Outline each blood parasite and name the species.
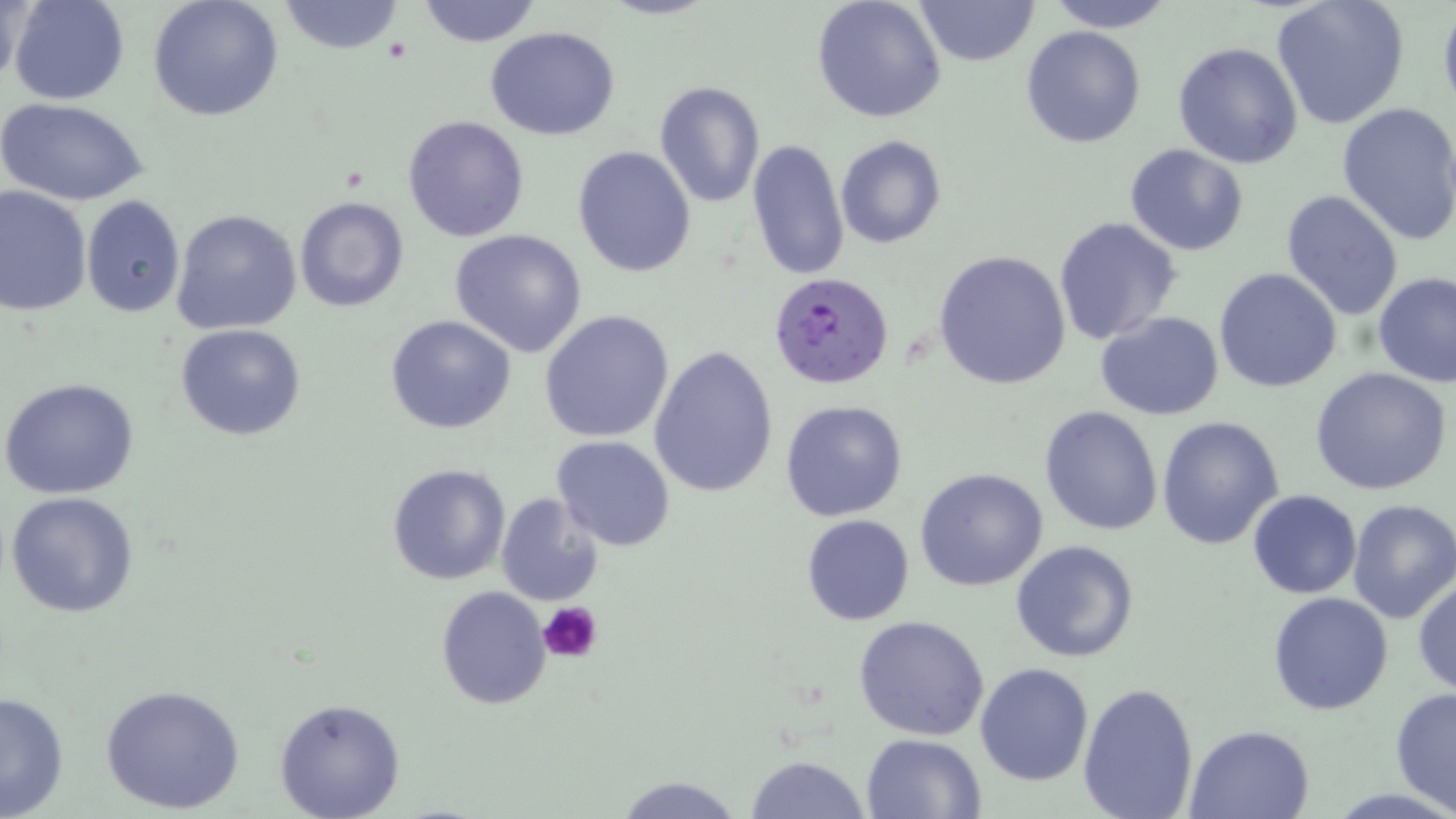
Approximate bounding boxes as (x1, y1, x2, y2) in pixels.
Plasmodium falciparum-infected red blood cells: (770, 272, 893, 390).
No Plasmodium ovale, Plasmodium malariae, Plasmodium vivax, Babesia divergens, or Trypanosoma brucei observed.

Uninfected red blood cell locations: (2, 0, 31, 85), (8, 0, 129, 106), (148, 0, 284, 122), (276, 0, 408, 54), (415, 0, 542, 48), (812, 0, 948, 123), (913, 0, 1040, 67), (1045, 0, 1177, 32), (1270, 0, 1410, 130), (1437, 2, 1456, 123), (484, 26, 623, 141), (1021, 26, 1147, 149), (1173, 41, 1303, 169), (653, 80, 765, 209), (1, 96, 150, 207), (1337, 101, 1456, 244), (402, 116, 530, 241), (834, 134, 946, 247), (745, 138, 850, 282), (1125, 144, 1250, 255), (572, 145, 697, 278), (0, 185, 93, 317), (1279, 189, 1403, 323), (294, 195, 410, 313), (81, 196, 185, 317), (171, 207, 302, 336), (1053, 217, 1182, 345), (449, 228, 588, 357), (933, 249, 1072, 390), (1214, 267, 1343, 393), (1373, 271, 1455, 387), (540, 310, 674, 444), (1095, 311, 1223, 421), (385, 315, 517, 435), (176, 324, 308, 441), (649, 343, 779, 498), (1310, 366, 1454, 497), (1, 379, 141, 500), (780, 399, 908, 521), (1039, 405, 1164, 536), (1156, 415, 1284, 550), (551, 436, 675, 552), (386, 463, 511, 586), (915, 468, 1049, 592), (5, 490, 140, 618), (1247, 490, 1361, 599), (495, 492, 607, 608), (1346, 498, 1456, 625), (801, 514, 915, 625), (1011, 539, 1141, 663), (1413, 577, 1456, 697), (434, 586, 552, 708), (1267, 591, 1394, 716), (853, 614, 990, 740), (974, 663, 1093, 786), (1077, 680, 1200, 818), (99, 683, 246, 815), (1390, 686, 1456, 817), (0, 689, 70, 819), (274, 697, 405, 819), (1184, 723, 1316, 817), (862, 733, 986, 819), (744, 754, 873, 818), (613, 775, 744, 818). Platelet locations: (538, 602, 603, 664). Slide-level diagnosis: Plasmodium falciparum. Optical microscopy. May-Grünwald-Giemsa-stained preparation. Image is 1456×819 pixels. Thin blood film. 1000x magnification. One field of a larger specimen.